Comment on the morphology of the red blood cells.
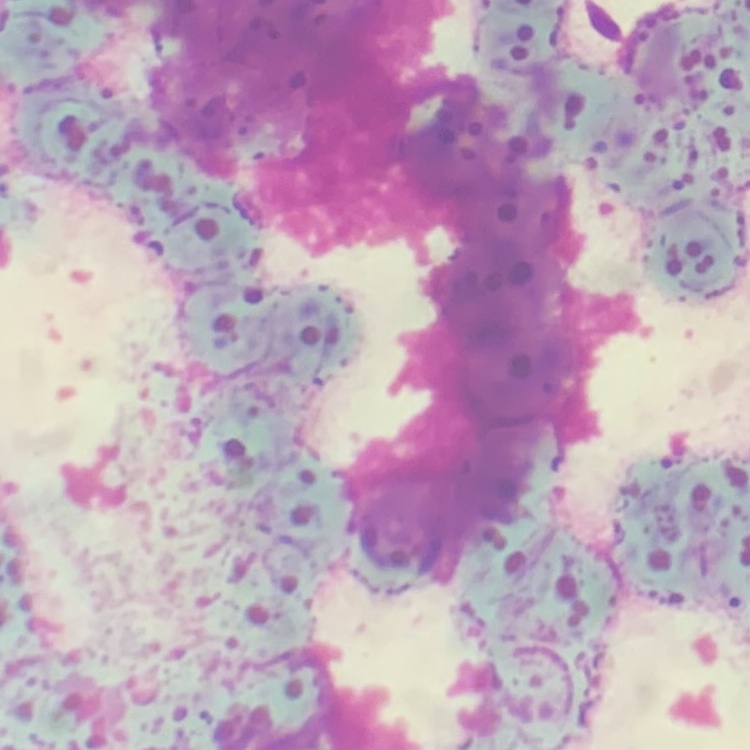
They show rouleaux formation.

Square crop of a larger photomicrograph. Thin blood smear. Field's or Giemsa stain.